State which parasite is depicted.
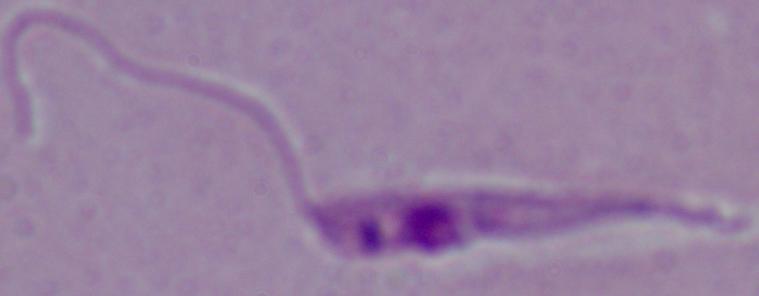

This is Leishmania.

magnification: 1000x
modality: micrograph